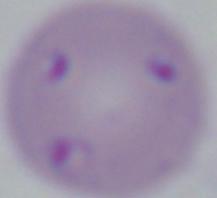

modality = photomicrograph
magnification = 1000x
identification = Babesia